Report the malaria status of this cell.
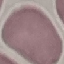
It is uninfected.

Giemsa-stained preparation. Acquired by smartphone through the microscope eyepiece. Automatically extracted cell patch, resized to 64 × 64 pixels. Thin smear of blood.